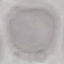

Result: no malaria parasites seen. Giemsa stain. Automatically extracted cell patch, resized to 64 × 64 pixels. Thin blood smear. Photographed with a smartphone camera at the microscope eyepiece.